Locate every malaria parasite.
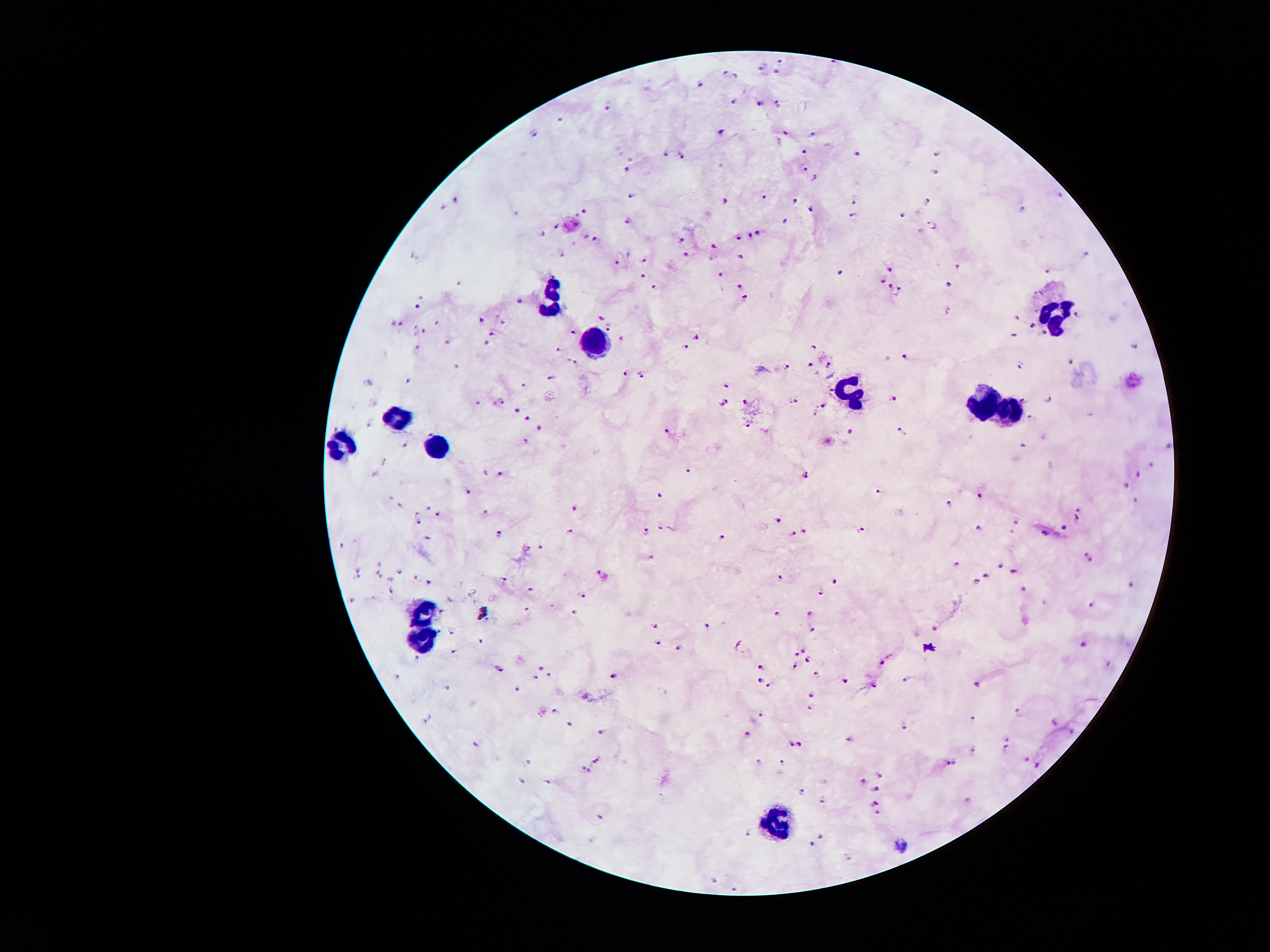

Approximate centers as [x, y] in pixels.
Malaria parasites: [781, 60], [835, 62], [761, 67], [724, 71], [774, 71], [737, 76], [700, 82], [737, 99], [779, 102], [759, 104], [609, 106], [559, 118], [722, 131], [786, 131], [813, 133], [535, 134], [804, 149], [666, 153], [858, 153], [939, 153], [682, 155], [806, 166], [624, 168], [937, 173], [816, 176], [1061, 195], [628, 196], [766, 196], [455, 198], [796, 198], [855, 200], [927, 200], [725, 202], [441, 207], [811, 208], [584, 210], [1023, 210], [853, 215], [903, 215], [630, 218], [787, 218], [934, 223], [557, 225], [544, 232], [584, 233], [759, 233], [596, 235], [749, 235], [739, 237], [680, 240], [715, 247], [687, 252], [1088, 252], [740, 254], [562, 255], [646, 259], [619, 260], [957, 264], [892, 269], [1048, 270], [643, 274], [841, 274], [722, 275], [882, 279], [462, 282], [739, 282], [950, 282], [656, 285], [888, 285], [900, 289], [744, 299], [522, 301], [416, 306], [947, 312], [1078, 312], [480, 316], [599, 317], [1016, 317], [502, 321], [394, 322], [438, 322], [401, 324], [418, 324], [1033, 324], [608, 326], [423, 331], [492, 331], [574, 331], [693, 334], [1046, 334], [1014, 336], [621, 338], [450, 339], [487, 343], [416, 346], [683, 346], [813, 346], [1135, 346], [561, 348], [907, 354], [1071, 361], [574, 363], [458, 364], [787, 364], [809, 364], [830, 366], [1021, 366], [626, 373], [641, 375], [552, 380], [371, 381], [411, 381], [522, 385], [729, 385], [502, 398], [747, 400], [794, 400], [1023, 400], [1050, 400], [727, 401], [897, 401], [473, 403], [824, 405], [517, 408], [816, 415], [1029, 416], [525, 418], [369, 423], [749, 425], [537, 427], [667, 430], [431, 432], [853, 432], [898, 432], [524, 442], [403, 445], [1023, 445], [1169, 447], [1152, 467], [687, 469], [374, 474], [485, 474], [806, 474], [1139, 474], [504, 475], [1127, 485], [882, 490], [468, 492], [979, 492], [658, 494], [1137, 499], [401, 504], [949, 505], [428, 507], [1080, 507], [487, 509], [574, 509], [438, 516], [1080, 517], [776, 521], [1018, 521], [418, 522], [1065, 527], [572, 529], [643, 529], [660, 529], [979, 529], [804, 531], [498, 532], [858, 532], [1046, 532], [796, 534], [428, 536], [724, 536], [341, 544], [540, 547], [650, 551], [1088, 556], [959, 561], [379, 563], [1003, 564], [359, 569], [1018, 569], [401, 571], [603, 573], [379, 574], [986, 574], [413, 576], [779, 576], [359, 578], [391, 579], [504, 579], [835, 579], [979, 579], [428, 583], [1023, 586], [1127, 586], [530, 588], [391, 591], [819, 591], [584, 594], [352, 601], [1090, 605], [441, 611], [485, 611], [574, 611], [776, 611], [809, 613], [656, 626], [707, 626], [813, 628], [934, 628], [441, 631], [453, 631], [480, 638], [658, 640], [735, 640], [1082, 643], [453, 648], [677, 648], [801, 648], [796, 655], [416, 657], [883, 660], [808, 662], [761, 663], [794, 665], [540, 667], [498, 668], [551, 673], [535, 675], [611, 675], [816, 677], [759, 678], [905, 678], [843, 682], [769, 684], [977, 684], [875, 685], [450, 687], [520, 689], [809, 692], [811, 705], [551, 709], [1019, 710], [762, 712], [428, 719], [971, 719], [1056, 722], [569, 724], [905, 725], [603, 731], [745, 732], [1075, 732], [1008, 737], [850, 739], [475, 741], [789, 744], [798, 746], [972, 749], [1006, 751], [598, 759], [1026, 759], [529, 761], [757, 762], [782, 762], [950, 762], [581, 764], [1036, 766], [589, 771], [882, 774], [520, 779], [549, 781], [863, 781], [877, 789], [801, 791], [821, 799], [875, 803], [601, 815], [745, 835], [821, 838], [809, 845], [848, 856], [715, 878], [735, 887].

Leukocyte locations: [1054, 298], [556, 306], [599, 339], [848, 387], [981, 404], [1008, 412], [398, 420], [347, 447], [439, 447], [420, 612], [423, 639], [772, 821]. 100x magnification. Giemsa stain. Patient malaria status: infected with Plasmodium falciparum. Smartphone photograph taken through the microscope eyepiece. Thick peripheral-blood smear. Image is 1270×952 pixels. One field from this slide.